State the preparation type.
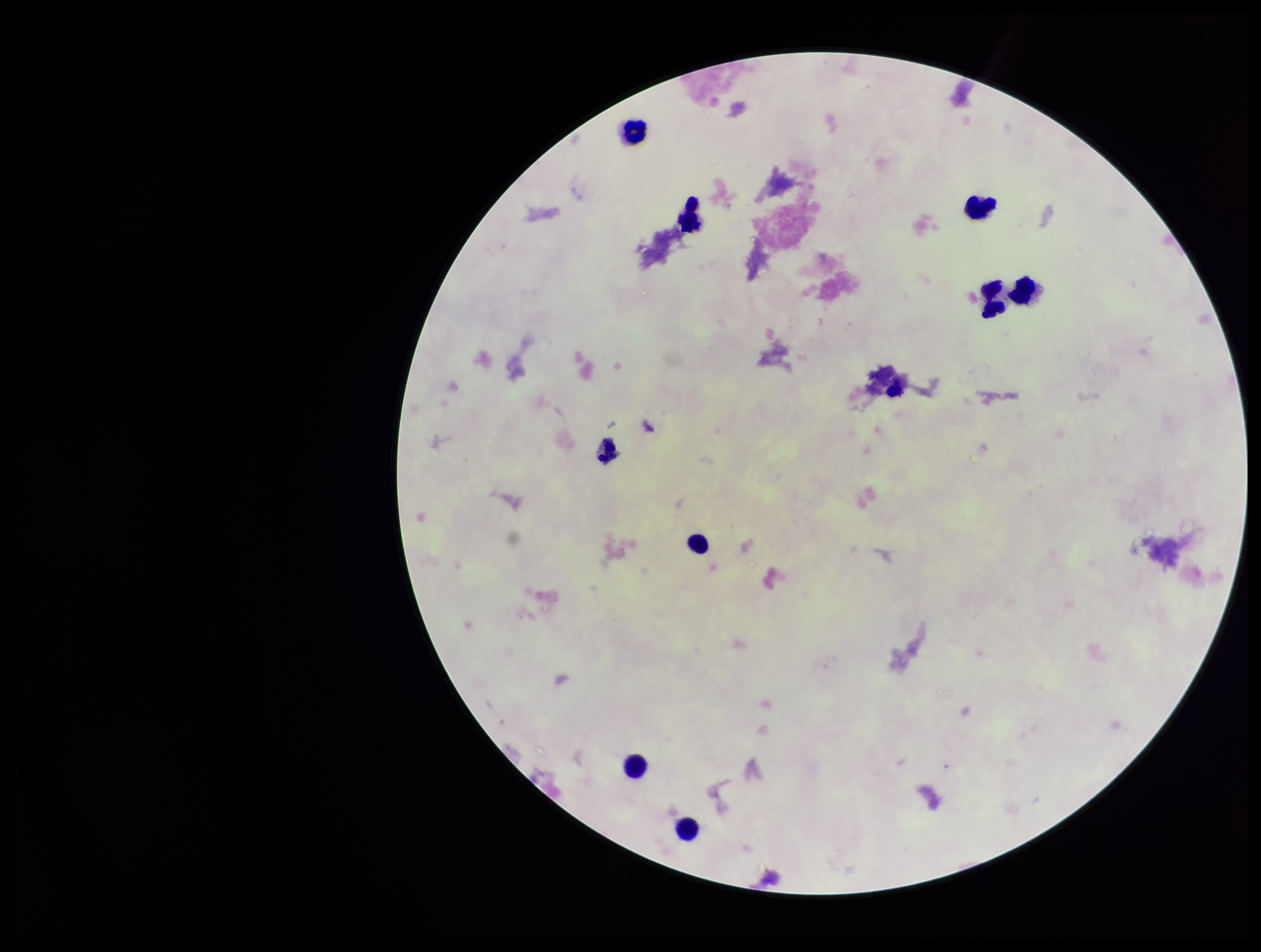

A thick smear.

{
  "patient_malaria_status": "negative",
  "plasmodium_parasites": "none detected",
  "field_of_view": "single",
  "stain": "Giemsa",
  "capture": "smartphone photograph through the microscope eyepiece",
  "image_size": "1261×952 pixels",
  "parasite_count": 0,
  "leukocyte_count": 9
}